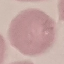
Malaria status: uninfected. Thin blood film. Automatically extracted cell patch, resized to 64 × 64 pixels. Acquired by smartphone through the microscope eyepiece. Giemsa stain.